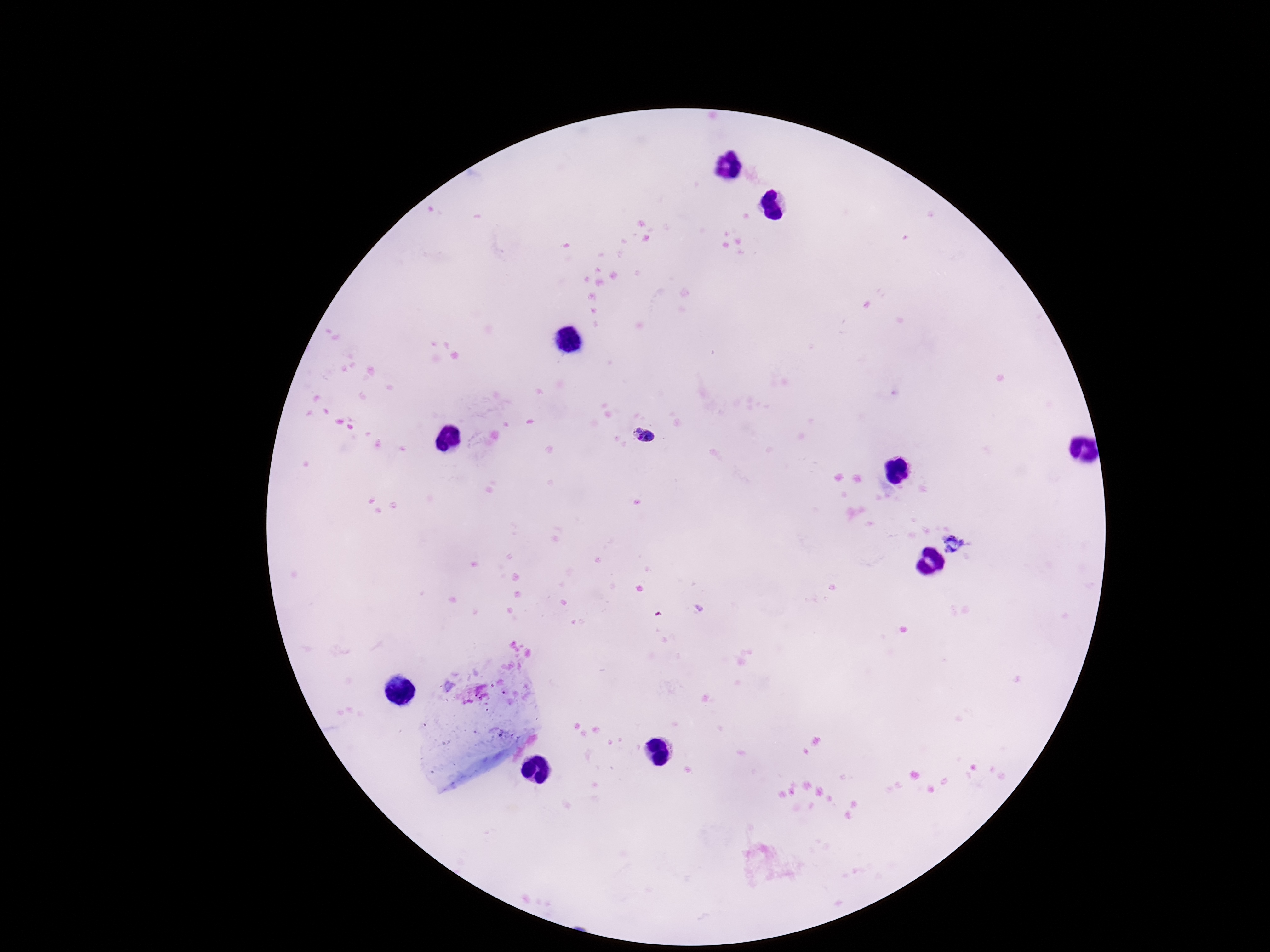

Approximate centers as (x, y) in pixels.
Summary:
  - Plasmodium parasite locations: (644, 436), (953, 544)
  - Preparation: thick peripheral-blood smear
  - Capture: smartphone camera through the microscope eyepiece
  - Stain: Giemsa
  - Image size: 1270×952 pixels
  - Magnification: 100x
  - Field of view: one from this slide
  - Patient malaria status: positive